Report the malaria status.
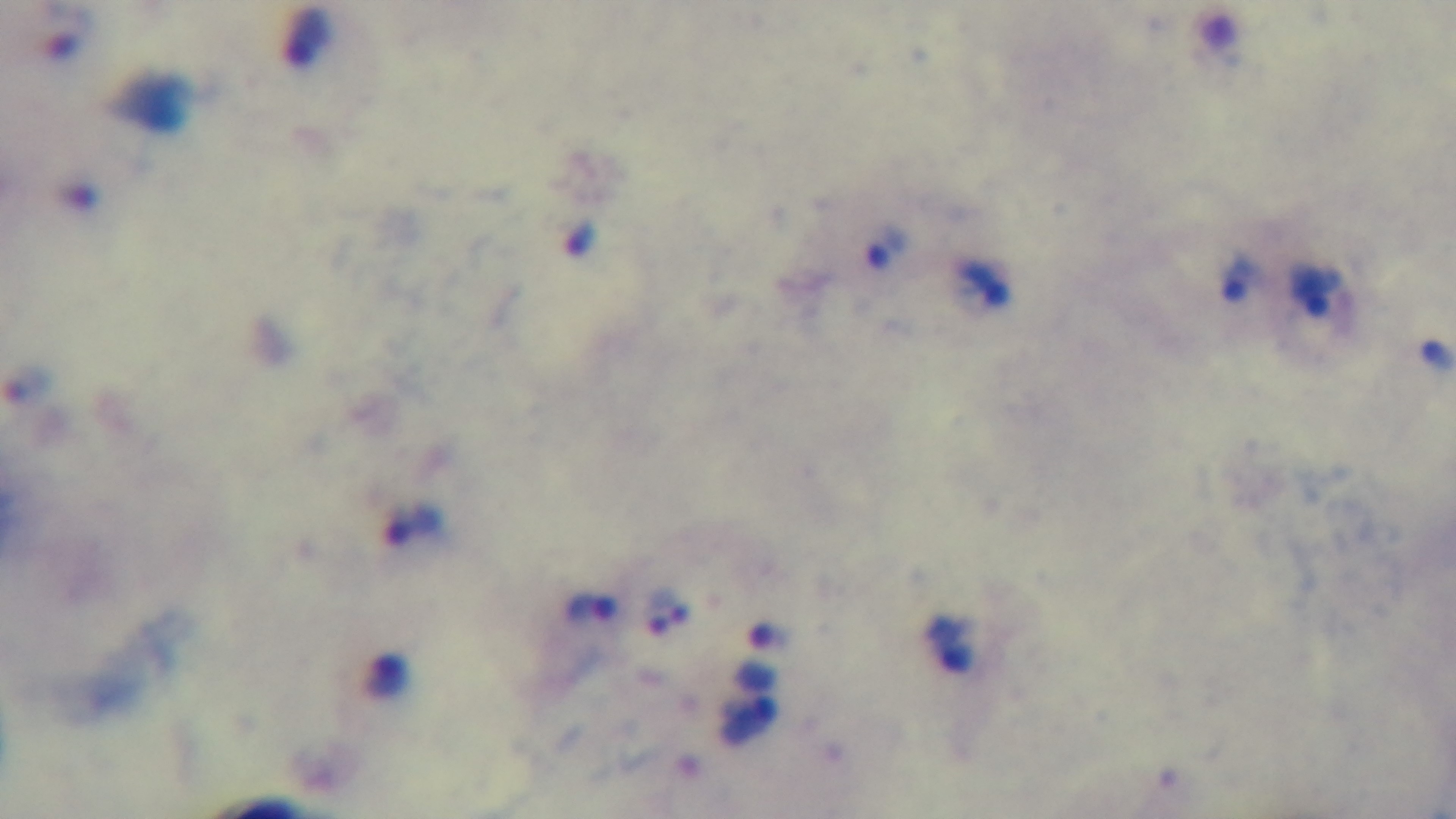

Infected.

Summary:
  - Stain: Giemsa
  - Objective: 100x oil immersion
  - Modality: light microscopy
  - Capture: mounted 4K digital camera
  - Field of view: one from the slide
  - Preparation: thick